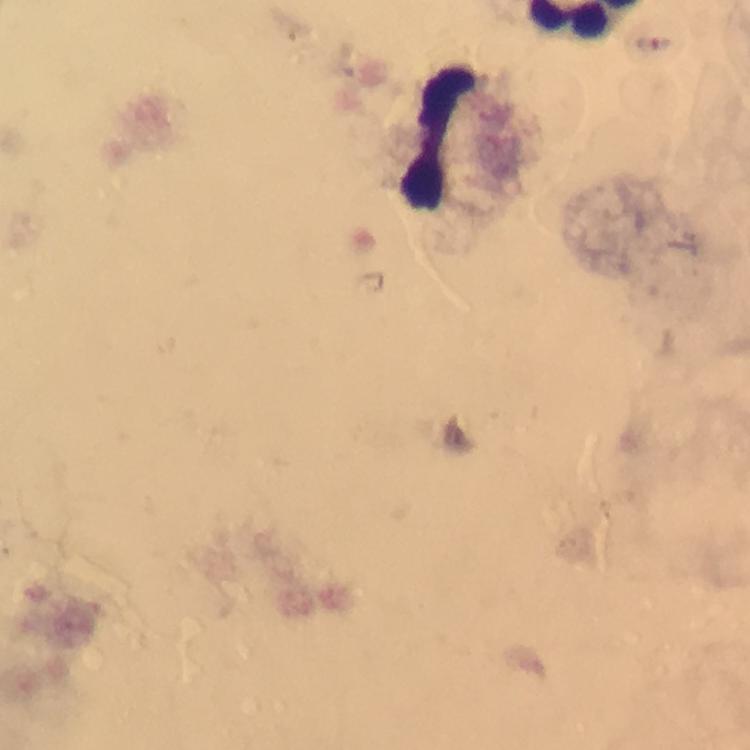

Approximate centers as [x, y] in pixels.
Summary:
  - Leukocyte locations: [439, 143]
  - Context: from a diagnostic examination for malaria
  - Magnification: 100x
  - Preparation: thick blood film
  - Malaria parasites: none seen
  - Capture: smartphone photograph through a microscope
  - Image size: 750×750 pixels
  - Cropped from: one field of view
  - Immersion oil: used
  - Stain: Giemsa